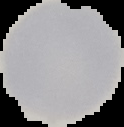

Summary:
  - Result: negative for Plasmodium parasites
  - Image type: cell region segmented out of the field of view; surrounding area masked to black
  - Preparation: thin blood smear
  - Image size: 124×127 pixels